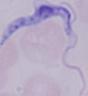
Micrograph. A trypanosome is seen. 1000x magnification.